Name the parasite shown.
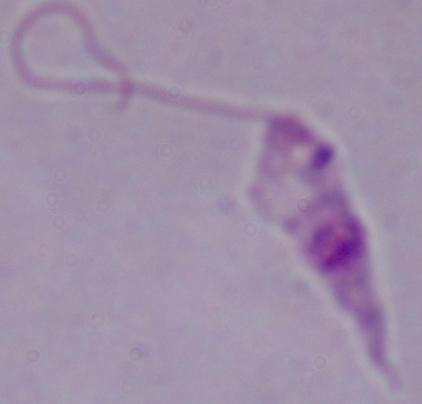
Leishmania.

magnification = 1000x
modality = micrograph